Identify the cell.
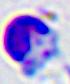
A leukocyte.

Photomicrograph. Captured at 400x magnification.